Identify the parasite.
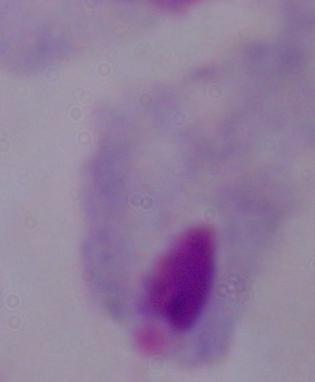

A trichomonad.

magnification = 1000x
modality = micrograph